Assess this cell for malaria.
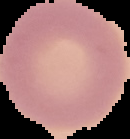

It is uninfected.

Summary:
  - Preparation: thin blood smear
  - Image size: 130×139 pixels
  - Image type: segmented cell region with the area outside set to black